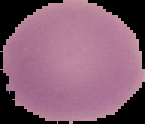
image_type: cell region segmented out of the field of view; surrounding area masked to black
image_size: 145×124 pixels
malaria_status: uninfected
preparation: thin blood smear